Classify the preparation.
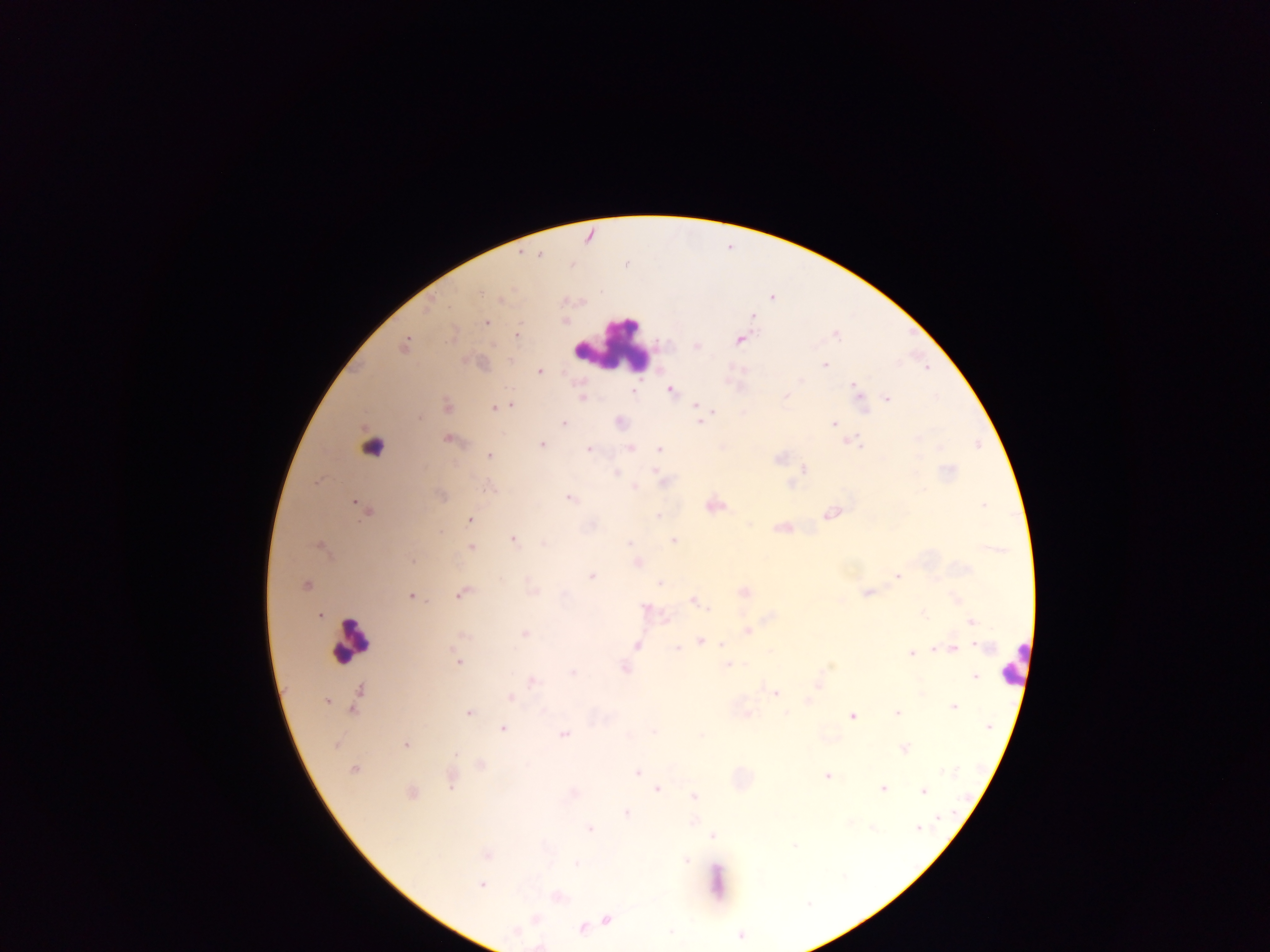

Thick blood smear.

image size = 1270×952 pixels
capture = mobile-phone photograph through a microscope
leukocyte locations = approximate centers as [x, y] in pixels: [613, 345], [355, 639]
Plasmodium parasite locations = approximate centers as [x, y] in pixels: [481, 291], [501, 299], [565, 320], [486, 322], [519, 334], [453, 336], [739, 340], [405, 345], [824, 366], [541, 370], [799, 381], [856, 387], [634, 391], [671, 392], [582, 395], [785, 396], [887, 398], [448, 404], [511, 405], [695, 405], [494, 408], [862, 409], [715, 411], [420, 417], [564, 422], [833, 423], [700, 424], [447, 438], [851, 441], [857, 442], [542, 444], [630, 447], [591, 448], [659, 449], [487, 455], [779, 457], [805, 467], [615, 473], [656, 473], [791, 485], [634, 487], [568, 498], [982, 504], [359, 507], [364, 511], [658, 515], [827, 515], [469, 519], [778, 528], [512, 540], [674, 540], [629, 543], [471, 547], [638, 564], [897, 575], [592, 577], [502, 580], [660, 582], [305, 583], [533, 591], [743, 591], [865, 593], [410, 596], [457, 596], [644, 607], [923, 614], [972, 622], [747, 631], [525, 634], [721, 644], [978, 646], [956, 648], [935, 649], [910, 654], [458, 662], [726, 665], [830, 665], [973, 676], [530, 680], [819, 682], [360, 689], [775, 693], [510, 697], [806, 700], [327, 701], [953, 706], [352, 710], [785, 711], [469, 712], [897, 712], [852, 716], [503, 728], [653, 731], [563, 735], [337, 743], [406, 744], [904, 749], [456, 754], [355, 770], [637, 773], [828, 775], [449, 788], [882, 788], [657, 789], [924, 790], [694, 795], [627, 813], [917, 828], [591, 830], [711, 835], [577, 863], [482, 885], [607, 920], [581, 928], [740, 935], [538, 946]
field of view = single
country = Ghana